Outline each Plasmodium falciparum-infected red blood cell.
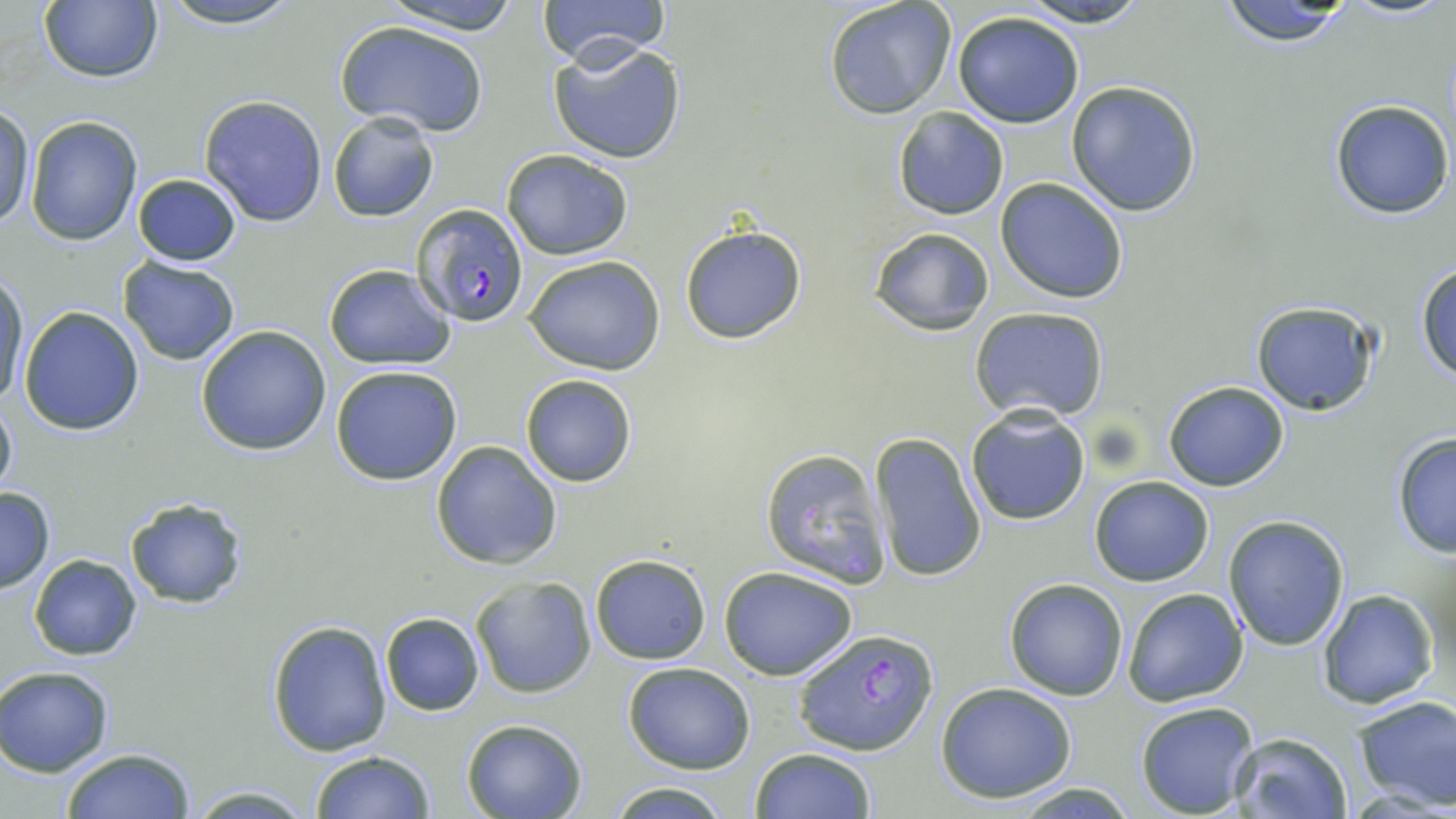
Approximate bounding boxes as (x1,y1)-(x2,y2) corner pairs in pixels.
Plasmodium falciparum-infected red blood cells: (412,203)-(532,328), (794,627)-(938,756).

slide-level diagnosis = Plasmodium falciparum
field of view = single
magnification = 1000x
preparation = thin blood film
uninfected red blood cell locations = approximate bounding boxes as (x1,y1)-(x2,y2) corner pairs in pixels: (39,0)-(163,83), (153,0)-(307,28), (380,0)-(526,34), (534,0)-(672,63), (1016,0)-(1156,27), (824,1)-(957,119), (1214,1)-(1358,48), (952,10)-(1086,128), (334,21)-(488,137), (548,41)-(687,164), (1065,80)-(1204,217), (200,94)-(328,227), (1328,98)-(1453,220), (1,102)-(35,230), (892,107)-(1010,221), (327,112)-(440,222), (25,115)-(142,246), (501,149)-(634,259), (130,173)-(244,267), (996,178)-(1129,304), (680,224)-(807,345), (869,227)-(993,333), (524,254)-(665,374), (117,258)-(240,366), (1414,261)-(1456,383), (323,263)-(456,368), (0,270)-(30,412), (1249,300)-(1381,417), (18,307)-(146,435), (970,308)-(1109,423), (194,326)-(332,455), (329,364)-(463,485), (519,373)-(637,487), (1162,380)-(1289,492), (0,391)-(18,504), (965,406)-(1091,527), (1390,432)-(1456,559), (869,433)-(988,586), (430,440)-(562,570), (759,447)-(891,587), (1089,476)-(1214,587), (0,486)-(56,595), (123,496)-(250,610), (1222,515)-(1350,651), (28,554)-(142,659), (589,554)-(710,664), (719,566)-(860,679), (471,576)-(596,698), (1003,577)-(1128,700), (1122,587)-(1249,708), (1316,589)-(1439,710), (380,612)-(484,715), (267,619)-(392,758), (622,662)-(756,774), (0,666)-(115,776), (935,682)-(1079,803), (1352,694)-(1456,812), (1134,701)-(1260,818), (462,718)-(587,819), (1230,731)-(1352,818), (61,747)-(196,819), (751,748)-(876,819), (311,750)-(432,819), (603,782)-(733,817), (1005,782)-(1141,816), (186,783)-(314,817)
modality = light microscopy
stain = May-Grünwald-Giemsa
image size = 1456×819 pixels